Report the malaria status of this cell.
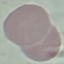
It is uninfected.

image_type: cell patch, automatically extracted from a larger field of view and resized to 64 × 64 pixels
preparation: thin smear
capture: smartphone camera at the microscope eyepiece
stain: Giemsa